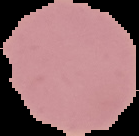

Summary:
  - Image size: 139×136 pixels
  - Preparation: thin blood smear
  - Malaria status: uninfected
  - Image type: cell region segmented out of the field of view; surrounding area masked to black